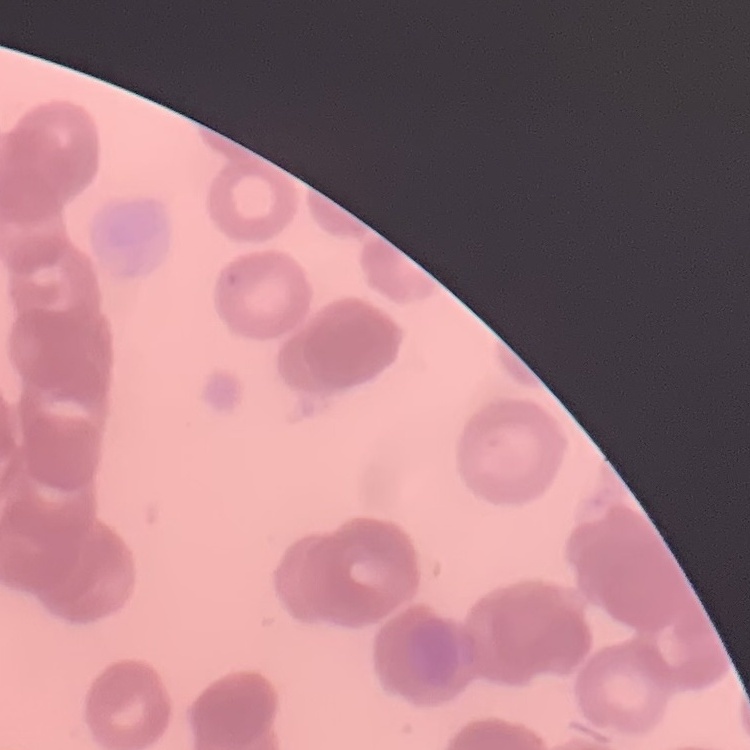
red blood cell morphology = rouleaux formation
image type = square crop of a larger photomicrograph
stain = Field's or Giemsa
preparation = thin blood film